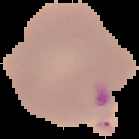 Image is 139×139 pixels. Malaria status: parasitized. Cell region segmented out of the field of view; the surrounding area is masked to black. From a thin blood smear.